State which cell type is depicted.
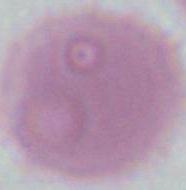
An erythrocyte.

modality = photomicrograph
magnification = 1000x